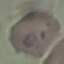
result: malaria parasites detected
stain: Giemsa
image_type: automatically extracted cell patch, resized to 64 × 64 pixels
preparation: thin blood film
capture: smartphone through the microscope eyepiece